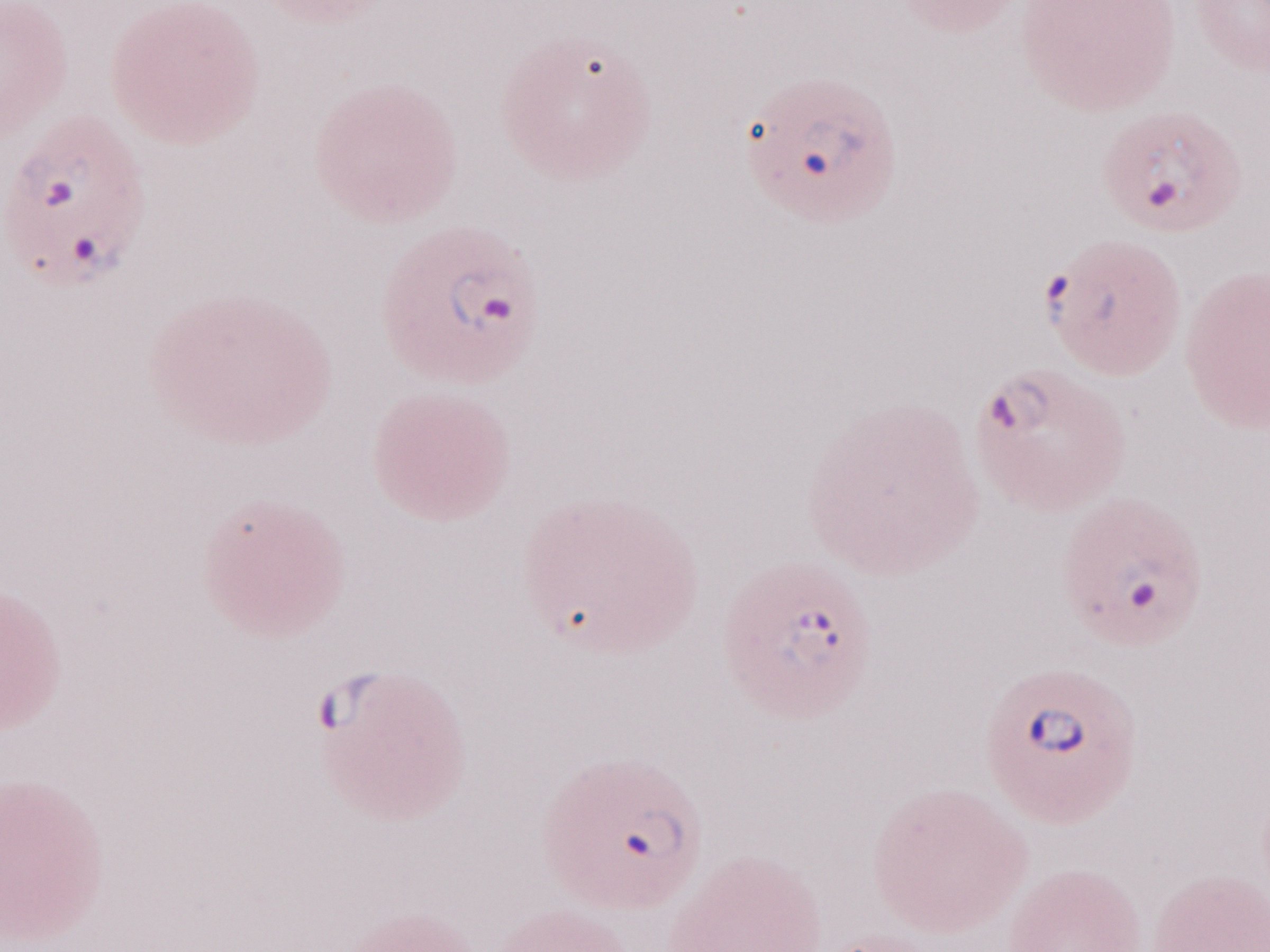
Thin blood film. Single field of view. Malaria diagnosis (patient-level): positive. Image is 1270×952 pixels. Olympus BX43 microscope, Olympus DP73 camera. Magnification: 1,000x. May-Grünwald-Giemsa (MGG) stain.